Outline platelets.
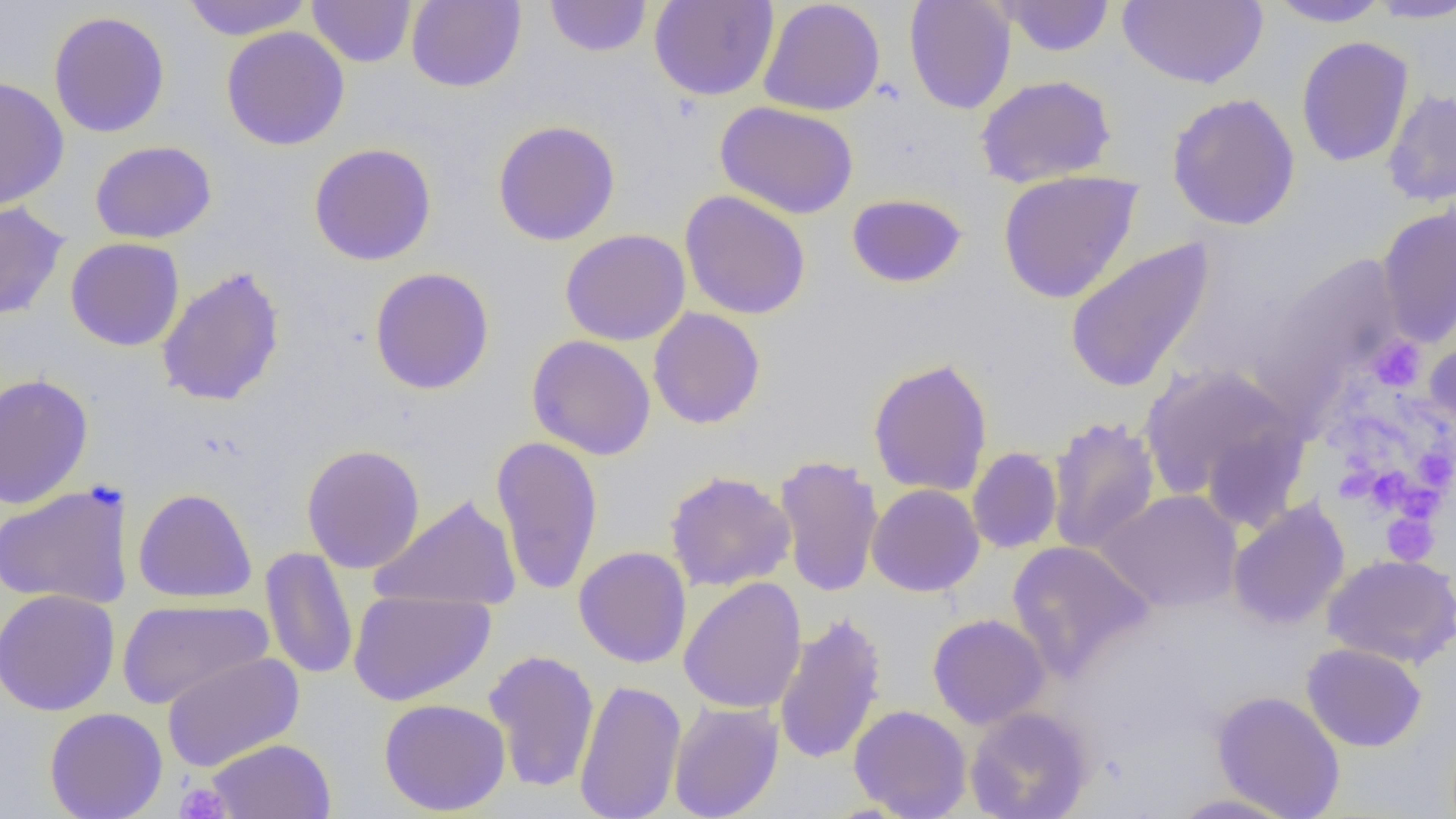

Approximate bounding boxes as (x1,y1)-(x2,y2) corner pairs in pixels.
Platelets: (1366,336)-(1426,393), (1412,446)-(1455,493), (1360,467)-(1414,515), (1382,513)-(1439,565), (175,781)-(232,819).

Uninfected red blood cell locations: (181,0)-(313,40), (306,0)-(417,67), (406,0)-(526,92), (544,0)-(652,57), (649,0)-(779,101), (758,0)-(886,116), (904,0)-(1016,114), (996,0)-(1115,56), (1119,0)-(1268,88), (1265,0)-(1393,28), (1367,0)-(1456,23), (48,11)-(170,138), (221,26)-(350,151), (1296,35)-(1414,167), (975,74)-(1116,187), (0,76)-(69,210), (1382,87)-(1456,208), (1166,93)-(1301,231), (715,100)-(859,219), (492,120)-(621,246), (90,140)-(217,244), (308,143)-(437,266), (997,170)-(1143,304), (679,190)-(811,320), (846,193)-(967,288), (0,201)-(69,321), (1376,205)-(1456,349), (559,228)-(690,346), (65,237)-(185,352), (1064,237)-(1215,394), (1260,254)-(1403,401), (156,265)-(286,407), (369,267)-(495,395), (648,307)-(765,429), (1424,334)-(1456,444), (526,335)-(656,460), (867,357)-(994,497), (1137,362)-(1310,522), (0,373)-(94,510), (1046,415)-(1161,555), (490,436)-(603,595), (301,443)-(425,574), (967,447)-(1063,554), (773,454)-(885,598), (665,470)-(796,592), (0,482)-(135,610), (867,483)-(984,597), (133,487)-(257,604), (1095,489)-(1243,613), (371,494)-(521,611), (1227,498)-(1350,631), (1007,540)-(1154,679), (574,546)-(693,668), (260,547)-(358,680), (1322,554)-(1456,669), (678,577)-(807,714), (0,588)-(120,716), (348,589)-(496,706), (116,598)-(272,709), (773,611)-(888,765), (928,613)-(1050,729), (1301,643)-(1427,752), (483,649)-(600,793), (161,652)-(304,772), (574,677)-(687,819), (1211,690)-(1345,819), (378,698)-(511,816), (668,701)-(784,819), (849,704)-(972,818), (965,706)-(1093,819), (44,707)-(168,818), (206,738)-(337,818), (1166,792)-(1300,818). Slide-level diagnosis: no evidence of blood parasites. Image is 1456×819 pixels. Thin blood film. Single field of view. 1000x magnification. Optical microscopy.